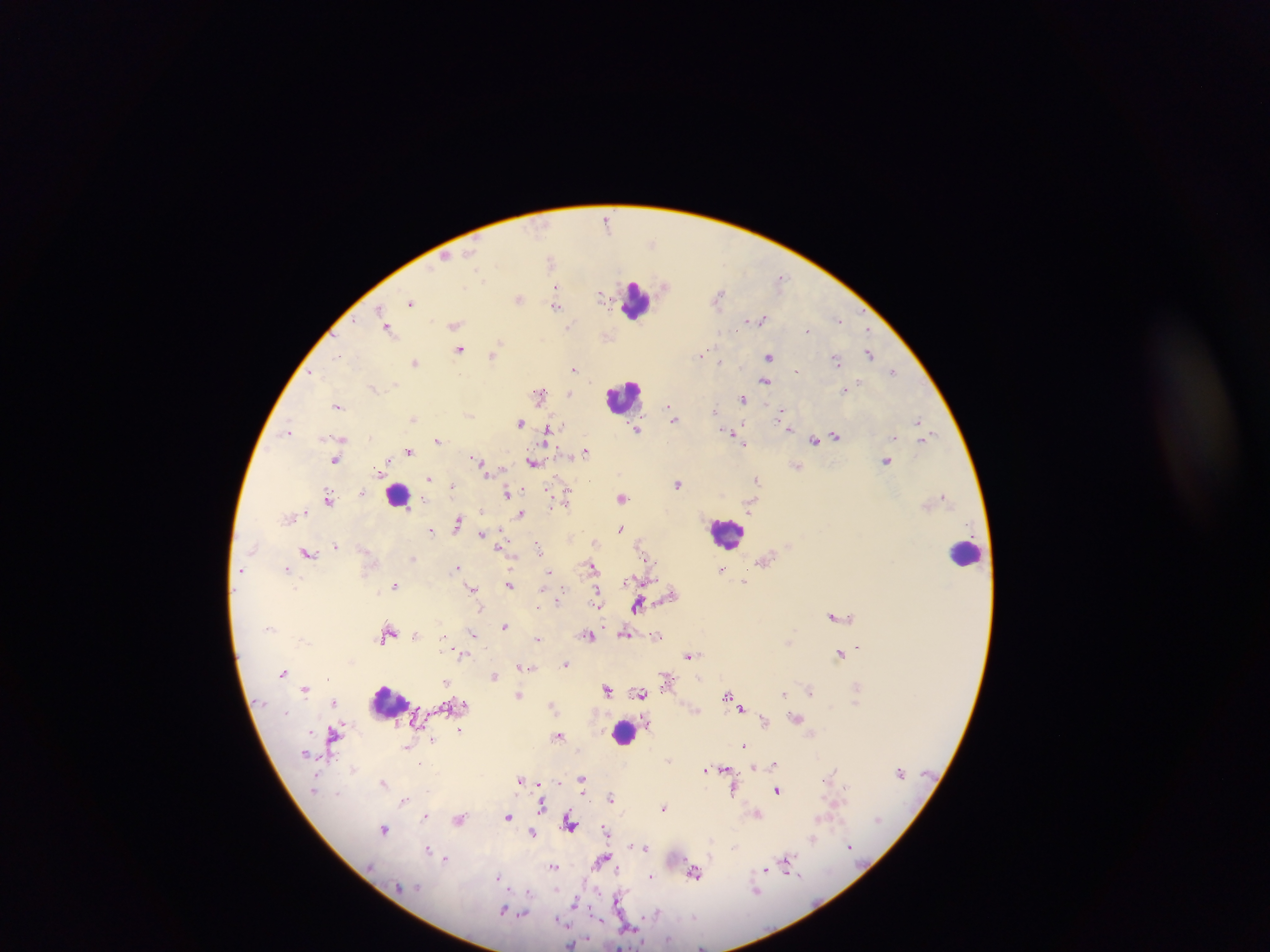

Approximate centers as (x, y) in pixels. Leukocyte locations: (637, 301), (621, 399), (396, 495), (733, 535), (965, 550), (388, 708), (623, 732). Malaria parasite locations: (607, 218), (655, 242), (445, 256), (550, 259), (557, 288), (719, 289), (602, 296), (410, 303), (557, 306), (760, 318), (838, 318), (455, 325), (568, 326), (389, 328), (807, 329), (866, 329), (497, 347), (457, 350), (703, 354), (869, 354), (338, 355), (493, 356), (768, 357), (836, 359), (719, 361), (417, 362), (575, 369), (893, 370), (766, 381), (395, 384), (634, 386), (373, 387), (569, 392), (538, 394), (742, 399), (338, 405), (670, 407), (716, 410), (778, 411), (470, 417), (673, 417), (415, 418), (916, 420), (519, 422), (788, 428), (547, 431), (638, 431), (286, 432), (730, 432), (920, 435), (836, 436), (369, 437), (342, 438), (439, 439), (814, 440), (743, 447), (586, 450), (409, 451), (475, 458), (534, 462), (886, 462), (336, 463), (378, 469), (430, 480), (757, 481), (677, 484), (328, 493), (507, 493), (942, 496), (566, 497), (623, 497), (328, 499), (751, 506), (481, 510), (520, 513), (459, 517), (457, 521), (622, 528), (433, 529), (480, 534), (500, 547), (539, 547), (308, 552), (514, 559), (592, 565), (288, 567), (456, 567), (547, 571), (628, 581), (649, 581), (394, 584), (512, 584), (471, 589), (542, 593), (598, 594), (560, 600), (636, 607), (480, 608), (600, 610), (832, 615), (504, 625), (389, 630), (416, 633), (473, 633), (591, 635), (626, 636), (791, 637), (387, 638), (538, 638), (445, 642), (789, 642), (858, 646), (840, 654), (465, 655), (689, 656), (567, 663), (530, 668), (283, 672), (496, 675), (327, 677), (700, 678), (446, 682), (381, 688), (306, 689), (607, 689), (811, 689), (640, 693), (783, 693), (520, 694), (726, 694), (336, 702), (552, 706), (742, 709), (287, 712), (646, 722), (765, 722), (337, 728), (459, 731), (310, 732), (559, 734), (331, 737), (432, 741), (745, 745), (305, 754), (419, 765), (725, 767), (755, 767), (352, 769), (704, 772), (520, 778), (582, 778), (559, 780), (384, 782), (315, 787), (776, 790), (733, 791), (338, 792), (583, 795), (611, 797), (403, 800), (544, 803), (663, 807), (758, 814), (424, 815), (509, 818), (875, 819), (459, 820), (878, 822), (571, 825), (606, 829), (385, 830), (532, 830), (814, 837), (712, 841), (630, 843), (734, 846), (645, 847), (849, 847), (428, 848), (446, 858), (603, 858), (787, 865), (553, 867), (615, 868), (765, 869), (694, 874), (496, 877), (650, 877), (529, 891), (756, 892), (619, 899), (575, 903), (619, 906), (501, 911), (655, 913), (524, 914), (629, 928), (570, 944), (701, 945). Image is 1270×952 pixels. Sample from Ghana. Photographed through a microscope with a mobile-phone camera. Thick blood smear. Single field of view.